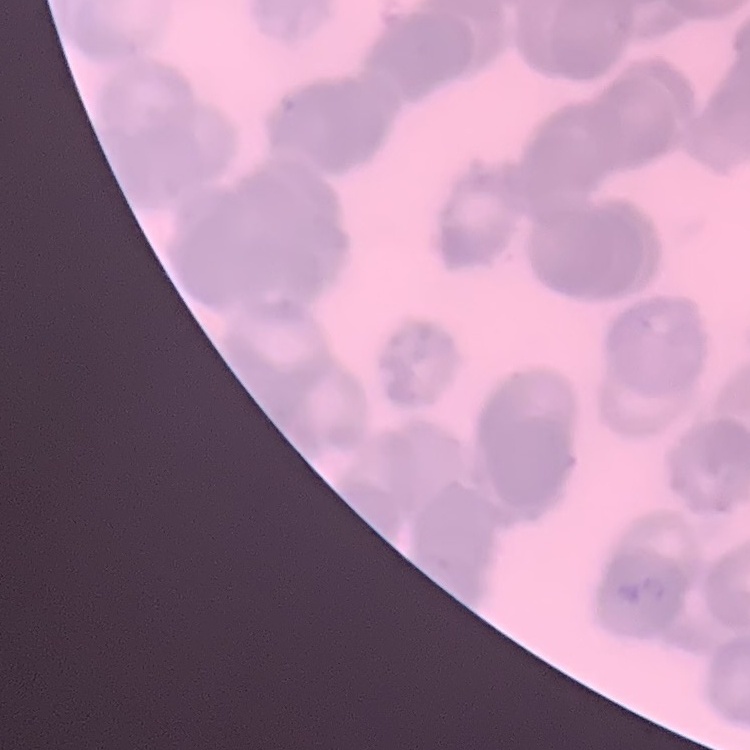
Summary:
  - Erythrocyte morphology: rouleaux formation
  - Image type: square crop of a larger photomicrograph
  - Preparation: thin blood film
  - Stain: Field's or Giemsa